State the blood parasite species.
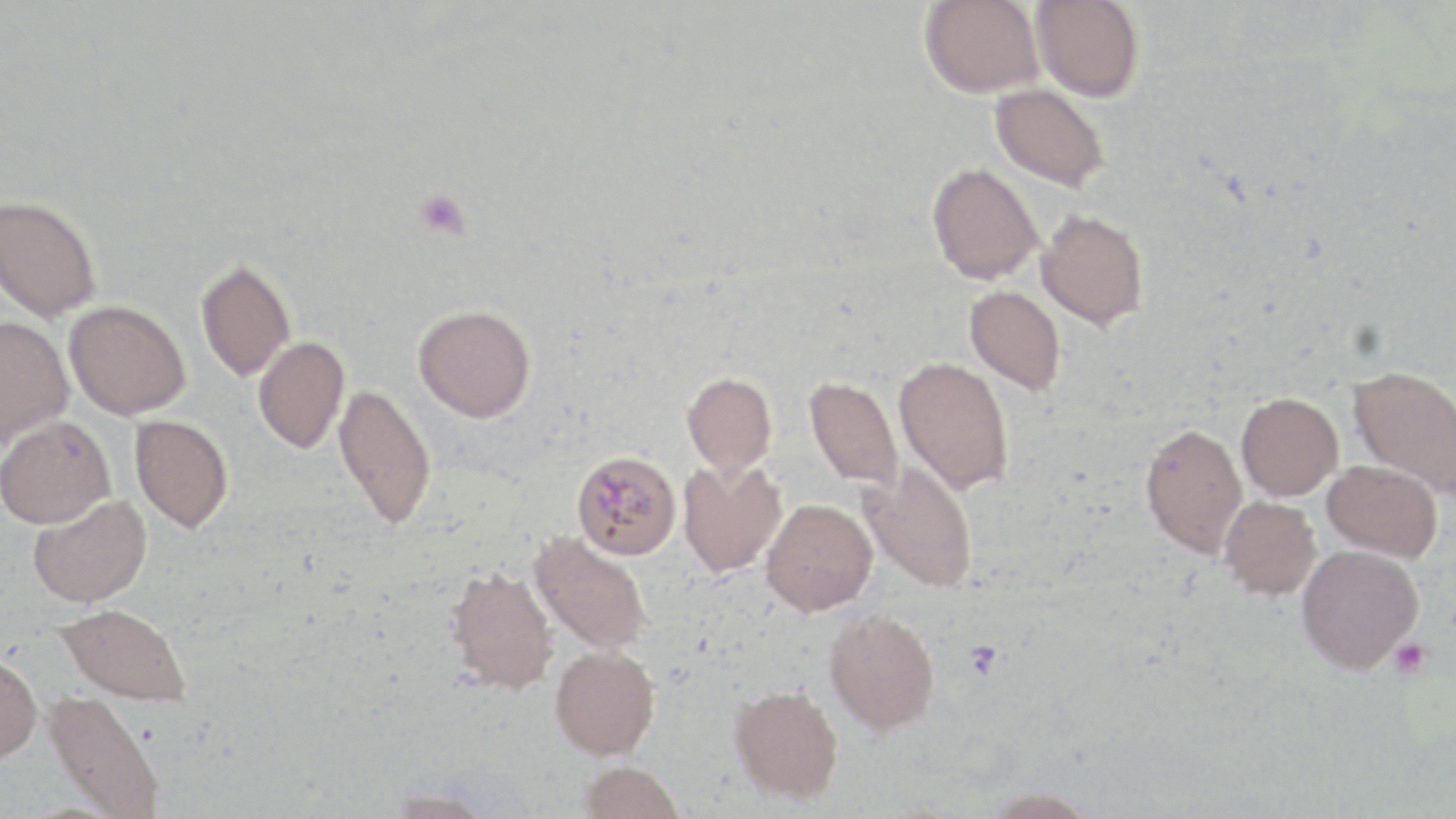
Plasmodium malariae.

Approximate bounding boxes as (x1,y1)-(x2,y2) corner pairs in pixels. Platelet locations: (413,189)-(471,240), (1388,638)-(1432,678). Uninfected red blood cell locations: (919,0)-(1044,98), (1031,0)-(1144,102), (990,84)-(1109,192), (926,162)-(1043,284), (0,194)-(102,322), (1036,208)-(1149,331), (194,257)-(296,382), (965,285)-(1066,395), (64,300)-(190,420), (413,304)-(536,422), (0,315)-(74,452), (253,336)-(349,454), (894,355)-(1013,495), (1347,365)-(1456,498), (681,371)-(777,479), (804,377)-(903,491), (333,383)-(437,531), (1236,392)-(1343,501), (130,414)-(233,534), (0,415)-(115,529), (1140,422)-(1248,558), (677,459)-(787,579), (1323,460)-(1443,561), (859,462)-(979,593), (27,494)-(152,608), (1219,496)-(1320,600), (761,499)-(877,615), (530,531)-(653,655), (1296,544)-(1423,674), (444,564)-(558,695), (55,603)-(192,706), (823,608)-(940,735), (550,645)-(660,760), (0,651)-(42,763), (729,684)-(844,805), (43,690)-(166,818), (578,760)-(684,819), (978,786)-(1101,818), (381,789)-(498,818). Plasmodium malariae-infected red blood cell locations: (572,450)-(681,559). Image is 1456×819 pixels. Captured at 1000x magnification. Light microscopy. Thin blood smear. One field of a larger specimen. May-Grünwald-Giemsa stain.